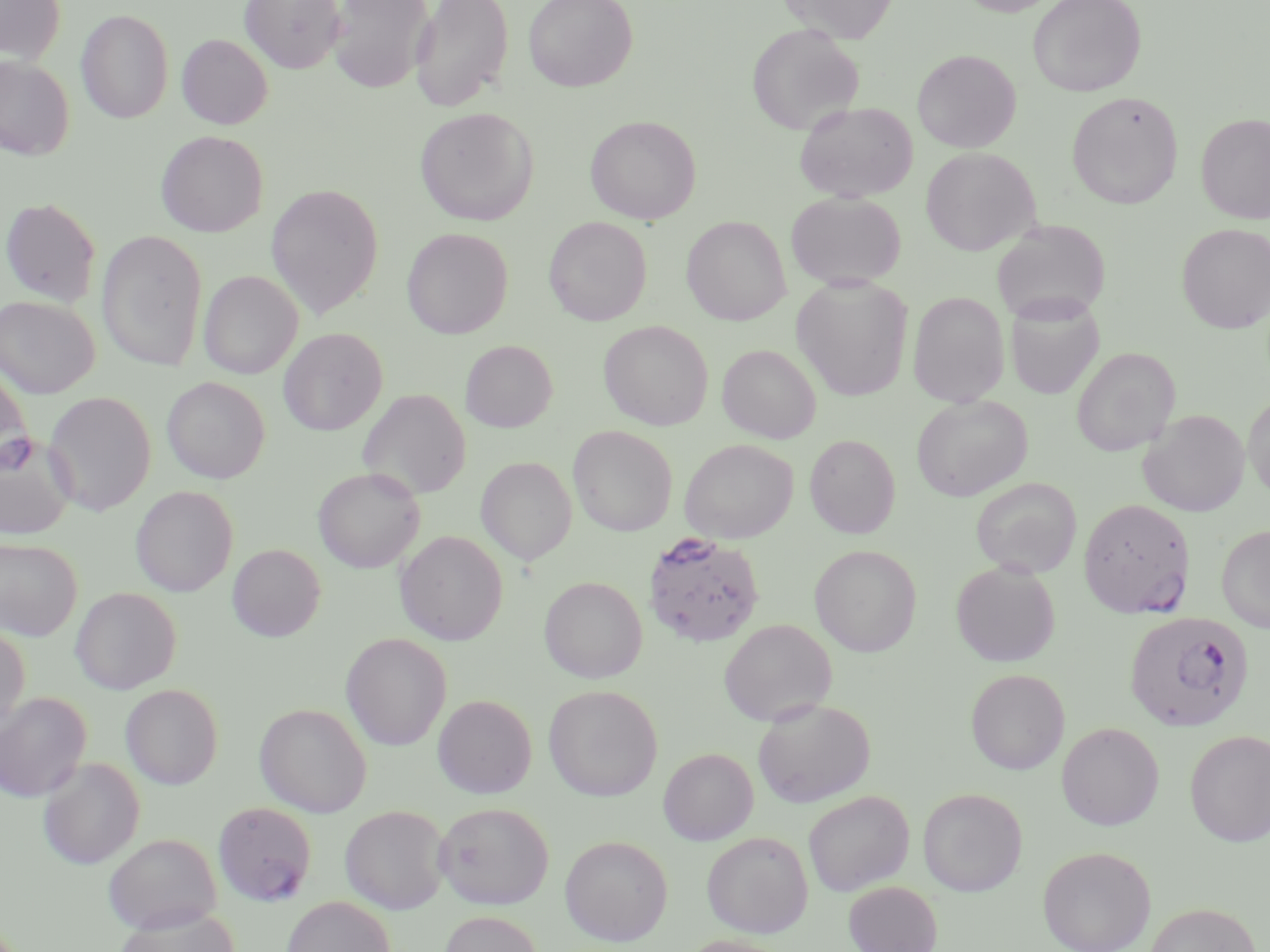

Summary:
  - Coordinate format: approximate bounding boxes as (x1, y1, x2, y2) in pixels
  - Plasmodium falciparum-infected red blood cell locations: (642, 531, 766, 647), (1124, 611, 1253, 732)
  - Uninfected red blood cell locations: (0, 0, 66, 64), (240, 0, 345, 73), (328, 0, 433, 92), (410, 0, 514, 112), (523, 0, 637, 91), (780, 0, 898, 42), (955, 0, 1062, 16), (1028, 0, 1146, 97), (76, 8, 174, 124), (746, 24, 863, 135), (176, 33, 274, 129), (912, 49, 1021, 153), (0, 55, 74, 160), (1066, 91, 1183, 209), (795, 101, 917, 202), (415, 107, 539, 226), (1196, 112, 1270, 225), (585, 115, 701, 224), (156, 130, 268, 237), (921, 147, 1039, 255), (266, 183, 384, 317), (786, 191, 907, 289), (0, 197, 101, 307), (682, 216, 791, 325), (544, 217, 652, 326), (991, 220, 1111, 324), (1177, 223, 1270, 334), (402, 228, 513, 339), (97, 230, 208, 372), (198, 270, 302, 379), (792, 275, 913, 401), (908, 292, 1009, 407), (0, 295, 99, 398), (1005, 297, 1103, 400), (599, 320, 713, 430), (279, 328, 387, 435), (460, 340, 557, 432), (717, 343, 821, 443), (1071, 347, 1179, 456), (0, 366, 32, 472), (162, 376, 270, 484), (359, 388, 470, 500), (43, 391, 156, 516), (1243, 392, 1270, 502), (911, 395, 1032, 502), (1138, 409, 1250, 516), (567, 425, 678, 536), (0, 432, 77, 540), (804, 434, 901, 538), (680, 438, 798, 543), (476, 456, 577, 565), (313, 467, 425, 573), (971, 477, 1082, 578), (131, 485, 238, 596), (1079, 497, 1196, 619), (1217, 524, 1270, 633), (395, 531, 508, 645), (0, 537, 83, 640), (227, 544, 325, 642), (810, 545, 922, 657), (951, 561, 1060, 667), (539, 576, 648, 684), (70, 586, 181, 694), (719, 619, 836, 726), (0, 625, 30, 732), (341, 633, 452, 751), (965, 669, 1069, 774), (120, 684, 223, 789), (543, 685, 662, 801), (0, 692, 91, 802), (433, 694, 537, 798), (752, 697, 875, 808), (254, 703, 372, 817), (1057, 722, 1164, 830), (1184, 730, 1270, 847), (658, 747, 758, 845), (38, 758, 145, 869), (918, 787, 1027, 896), (803, 791, 914, 896), (434, 801, 554, 909), (213, 802, 317, 906), (340, 805, 450, 914), (701, 831, 813, 938), (103, 833, 222, 934), (559, 835, 673, 946), (1037, 846, 1156, 952), (844, 881, 942, 952), (282, 896, 395, 952), (1145, 902, 1261, 952), (114, 905, 239, 952), (438, 910, 545, 952), (677, 935, 791, 952)
  - Slide-level diagnosis: Plasmodium falciparum
  - Stain: May-Grünwald-Giemsa
  - Preparation: thin blood film
  - Image size: 1270×952 pixels
  - Modality: light microscopy
  - Magnification: 1000x
  - Field of view: single